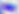 400x magnification. Toxoplasma gondii is shown. Photomicrograph.